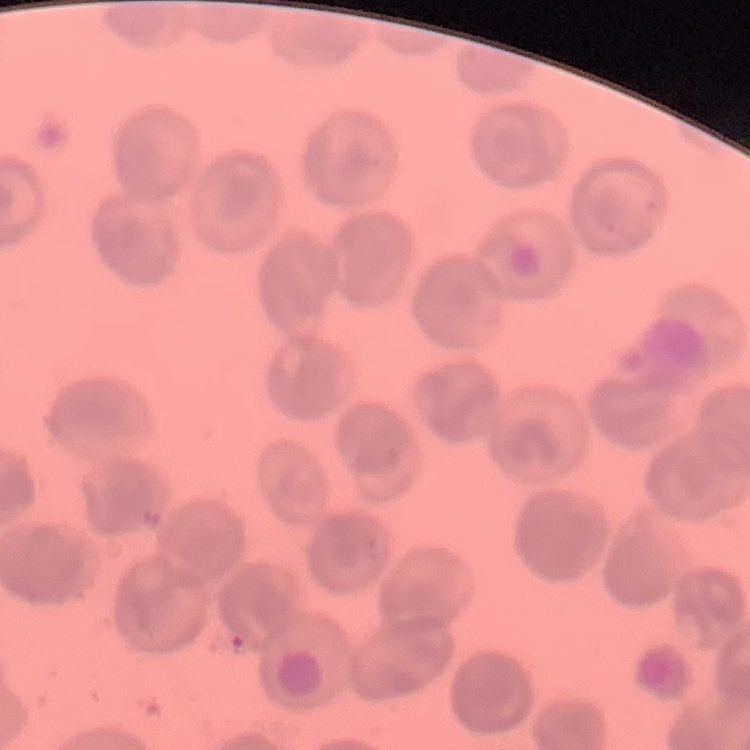
erythrocyte morphology = no rouleaux formation
stain = Field's or Giemsa
image type = one tile cut from a larger photomicrograph
preparation = thin blood film